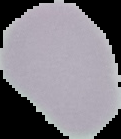

Result: no malaria parasites detected. From a thin blood smear. Segmented cell region on a black background. Image is 121×139 pixels.